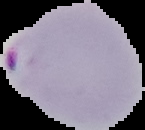
preparation = thin blood smear
result = Plasmodium parasites detected
image type = cell region segmented out of the field of view; surrounding area masked to black
image size = 145×130 pixels